Give the extent of all Plasmodium malariae-infected red blood cells.
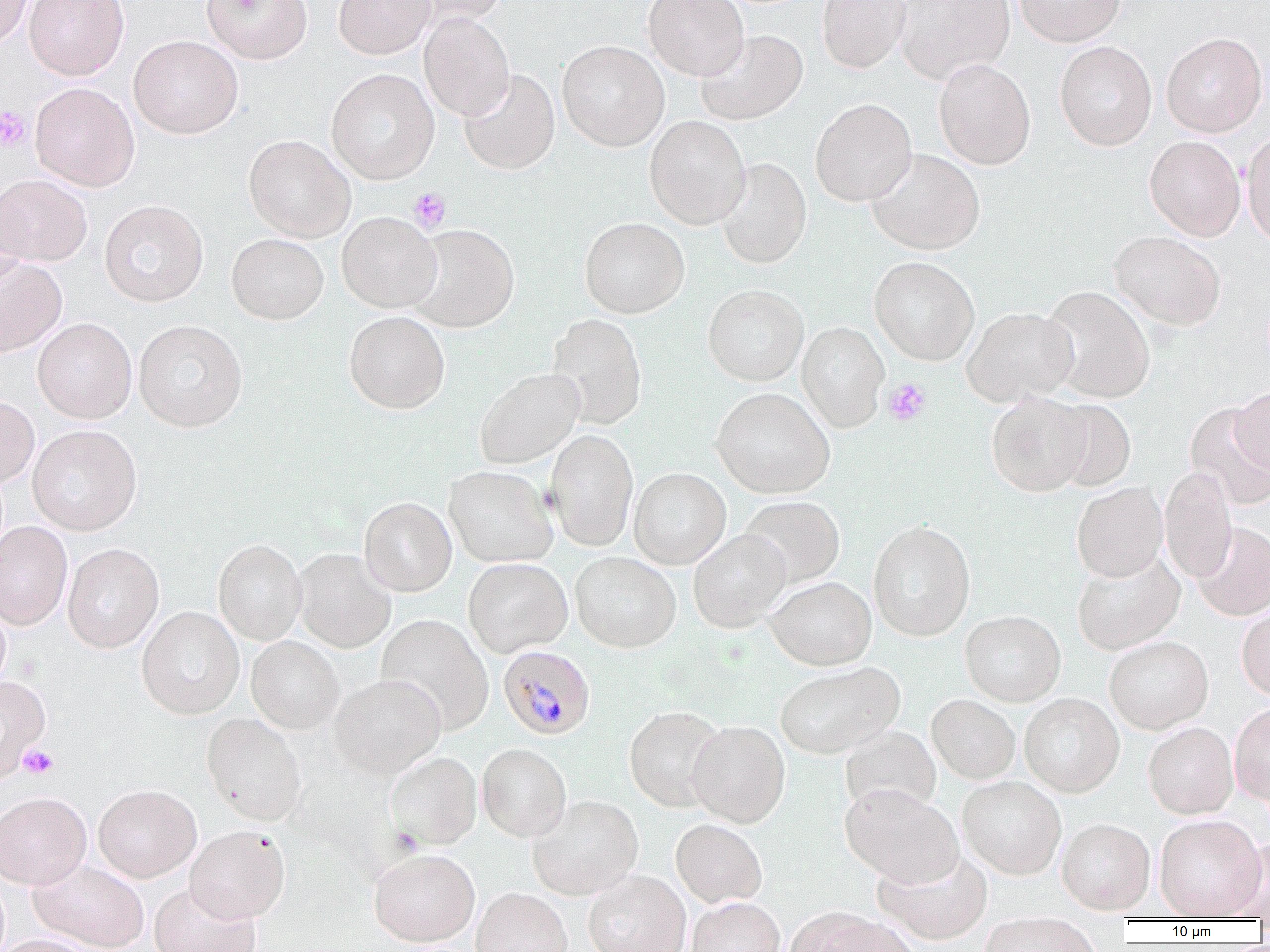
Approximate bounding boxes as [x1, y1, x2, y2] in pixels.
Plasmodium malariae-infected red blood cells: [498, 645, 596, 739].

Summary:
  - Platelet locations: [0, 106, 32, 151], [407, 187, 452, 233], [883, 378, 931, 426], [18, 743, 58, 779]
  - Uninfected red blood cell locations: [0, 0, 32, 50], [24, 0, 129, 80], [201, 0, 312, 63], [333, 0, 435, 59], [404, 0, 509, 24], [643, 0, 749, 80], [817, 0, 910, 73], [894, 0, 1015, 83], [1014, 0, 1125, 47], [419, 12, 515, 120], [696, 29, 808, 125], [1161, 32, 1268, 138], [129, 35, 243, 139], [557, 40, 670, 150], [1054, 40, 1157, 150], [933, 58, 1036, 169], [326, 68, 439, 184], [459, 69, 560, 174], [30, 82, 140, 191], [810, 98, 917, 206], [644, 116, 751, 229], [1241, 132, 1270, 248], [243, 135, 356, 242], [1144, 135, 1246, 241], [866, 147, 985, 255], [716, 157, 812, 269], [0, 174, 93, 266], [0, 189, 31, 290], [99, 200, 208, 307], [337, 211, 442, 313], [580, 216, 689, 319], [407, 223, 519, 332], [1110, 231, 1226, 330], [226, 233, 329, 325], [0, 255, 67, 356], [869, 256, 980, 365], [703, 284, 808, 386], [1040, 285, 1155, 403], [962, 307, 1079, 406], [343, 311, 450, 414], [547, 313, 647, 429], [32, 317, 137, 423], [133, 319, 248, 433], [797, 321, 889, 433], [474, 368, 584, 468], [1232, 386, 1270, 476], [712, 387, 835, 499], [986, 391, 1092, 496], [0, 395, 39, 487], [1048, 399, 1136, 492], [1185, 402, 1270, 509], [27, 425, 142, 535], [544, 428, 639, 552], [444, 466, 557, 568], [1160, 466, 1237, 583], [629, 468, 731, 569], [1072, 483, 1168, 582], [738, 496, 845, 588], [359, 497, 457, 596], [867, 520, 975, 641], [0, 521, 73, 630], [1192, 522, 1270, 621], [688, 529, 791, 633], [213, 539, 307, 645], [63, 543, 164, 653], [293, 548, 396, 652], [1071, 551, 1185, 655], [570, 552, 681, 652], [463, 558, 573, 658], [766, 576, 877, 671], [0, 598, 10, 693], [1236, 603, 1270, 700], [137, 606, 244, 719], [960, 611, 1065, 707], [376, 614, 494, 734], [246, 636, 344, 734], [1104, 636, 1213, 735], [775, 663, 904, 760], [330, 674, 445, 778], [0, 676, 51, 783], [926, 694, 1020, 784], [1020, 694, 1124, 797], [1230, 701, 1270, 806], [624, 706, 726, 812], [202, 713, 306, 826], [686, 721, 790, 827], [1143, 723, 1238, 820], [840, 726, 941, 817], [477, 744, 571, 842], [386, 751, 482, 850], [957, 777, 1066, 878], [93, 784, 202, 882], [840, 784, 964, 888], [0, 792, 92, 889], [527, 796, 643, 901], [1154, 817, 1265, 920], [670, 819, 767, 908], [1056, 819, 1156, 916], [185, 826, 290, 924], [1224, 838, 1270, 920], [368, 850, 480, 947], [873, 851, 994, 946], [29, 860, 149, 951], [584, 871, 690, 952], [148, 882, 261, 952], [471, 888, 572, 952], [686, 898, 786, 952], [798, 912, 921, 952], [978, 914, 1103, 952], [0, 934, 96, 952]
  - Slide-level diagnosis: Plasmodium malariae
  - Magnification: 1000x
  - Modality: light microscopy
  - Preparation: thin blood film
  - Field of view: single
  - Image size: 1270×952 pixels